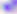

Captured at 400x magnification. Toxoplasma gondii is shown. Photomicrograph.